Locate every leukocyte (white blood cell).
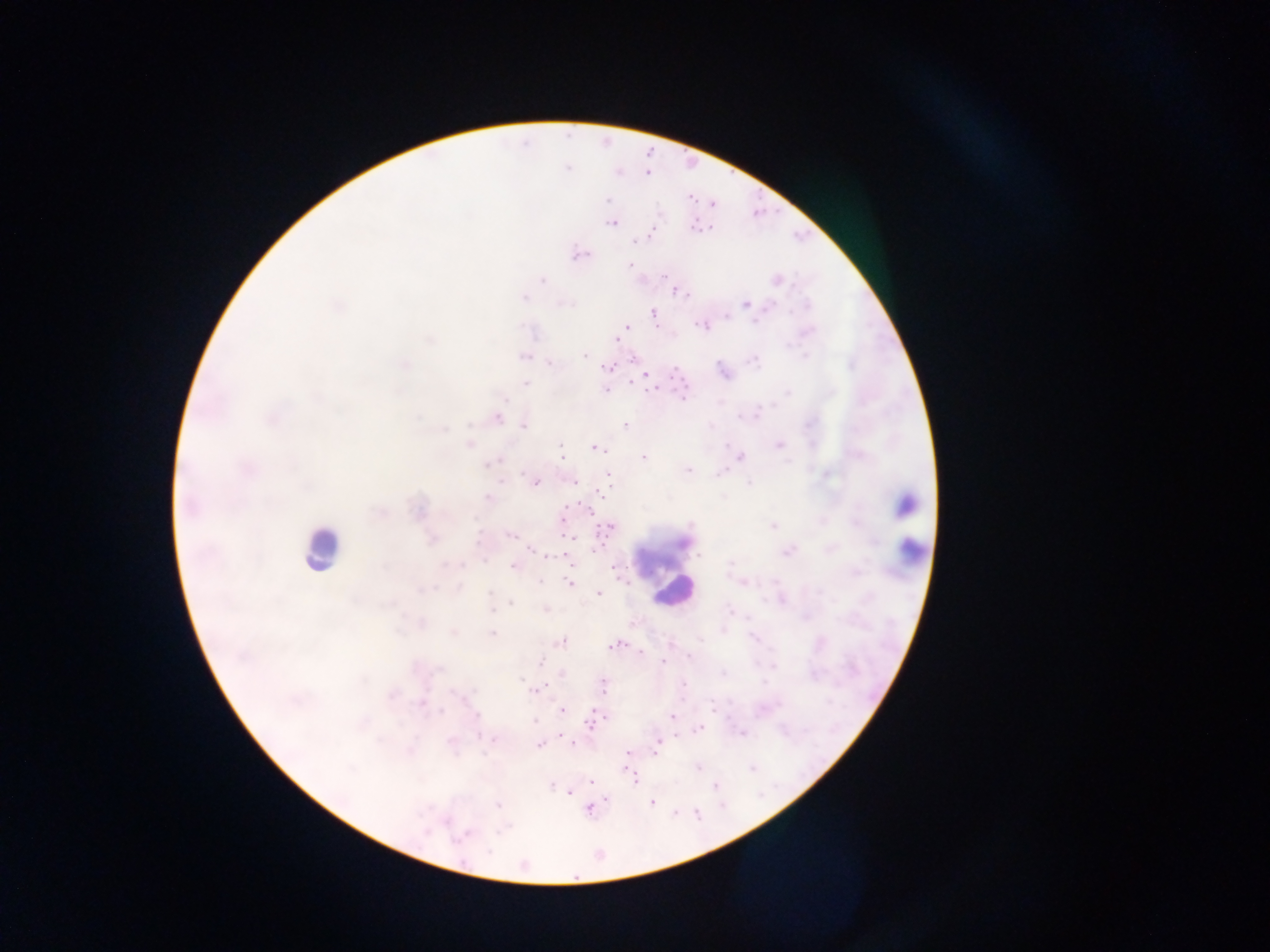

Approximate centers as (x, y) in pixels.
Leukocytes: (903, 505), (320, 548), (910, 548), (673, 591).

malaria_parasite_locations: 'approximate centers as (x, y) in pixels: (567, 168), (647, 174), (690, 198), (608, 200), (712, 203), (610, 223), (694, 226), (650, 233), (633, 242), (579, 254), (629, 264), (663, 275), (777, 280), (543, 281), (673, 289), (686, 294), (745, 304), (806, 305), (653, 313), (725, 317), (756, 321), (700, 325), (626, 326), (616, 339), (584, 356), (806, 356), (524, 357), (633, 358), (755, 361), (551, 363), (405, 365), (852, 365), (607, 368), (645, 375), (526, 383), (630, 383), (653, 388), (605, 390), (787, 393), (684, 397), (505, 400), (498, 418), (523, 425), (625, 427), (444, 430), (469, 444), (561, 444), (727, 445), (779, 445), (596, 448), (562, 457), (741, 457), (643, 458), (498, 459), (492, 462), (688, 470), (522, 474), (607, 474), (530, 480), (574, 482), (536, 483), (748, 484), (601, 492), (488, 497), (562, 519), (691, 525), (772, 525), (610, 527), (511, 536), (571, 537), (682, 542), (530, 550), (787, 553), (699, 556), (571, 563), (731, 564), (463, 565), (513, 566), (614, 567), (540, 580), (568, 584), (489, 593), (598, 594), (511, 604), (492, 610), (730, 611), (492, 634), (752, 638), (561, 641), (613, 646), (641, 652), (689, 656), (663, 661), (540, 662), (774, 666), (562, 673), (723, 673), (521, 680), (525, 684), (683, 685), (604, 686), (538, 689), (422, 703), (712, 707), (562, 710), (441, 711), (594, 715), (476, 716), (672, 716), (534, 721), (590, 723), (699, 729), (742, 733), (494, 739), (573, 744), (657, 744), (538, 745), (657, 749), (629, 752), (698, 767), (625, 768), (752, 768), (591, 781), (635, 781), (551, 786), (715, 786), (569, 793), (606, 798), (651, 802), (498, 805), (697, 814), (461, 837), (488, 851)'
country: Ghana
preparation: thick blood film
capture: mobile-phone photograph through a microscope
image_size: 1270×952 pixels
field_of_view: single